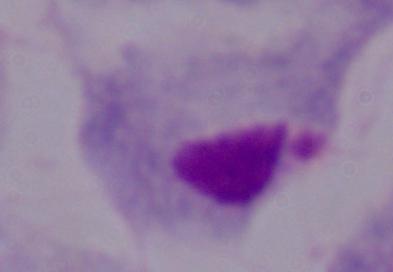
Summary:
  - Modality: photomicrograph
  - Magnification: 1000x
  - Identification: trichomonad